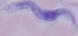
Summary:
  - Magnification: 1000x
  - Modality: photomicrograph
  - Identification: trypanosome